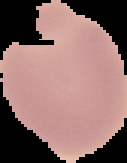

image type = segmented cell region with the area outside set to black
malaria status = uninfected
preparation = thin blood smear
image size = 127×163 pixels